Describe the morphology of the red blood cells.
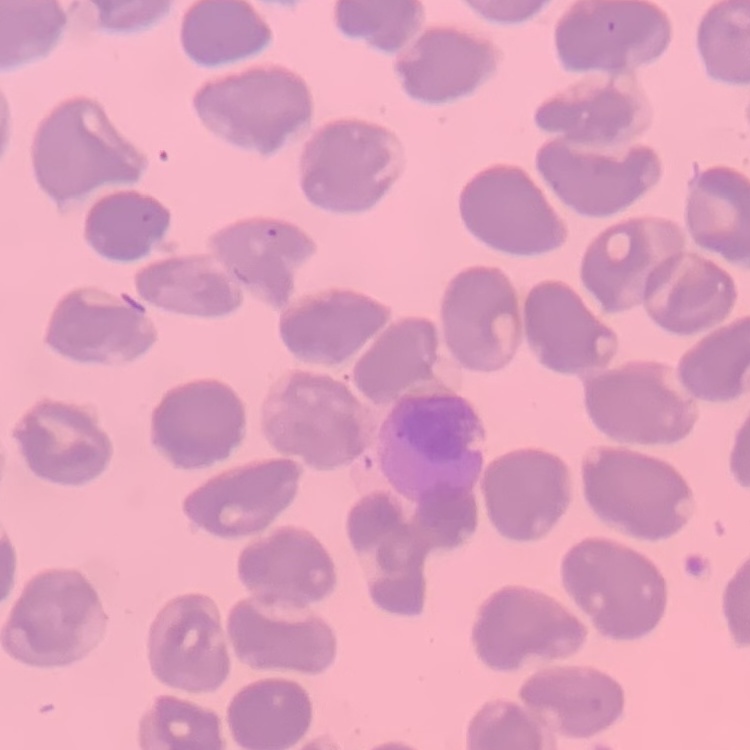

They show no rouleaux formation.

Summary:
  - Preparation: thin peripheral smear
  - Stain: Field's or Giemsa
  - Image type: square crop of a larger photomicrograph